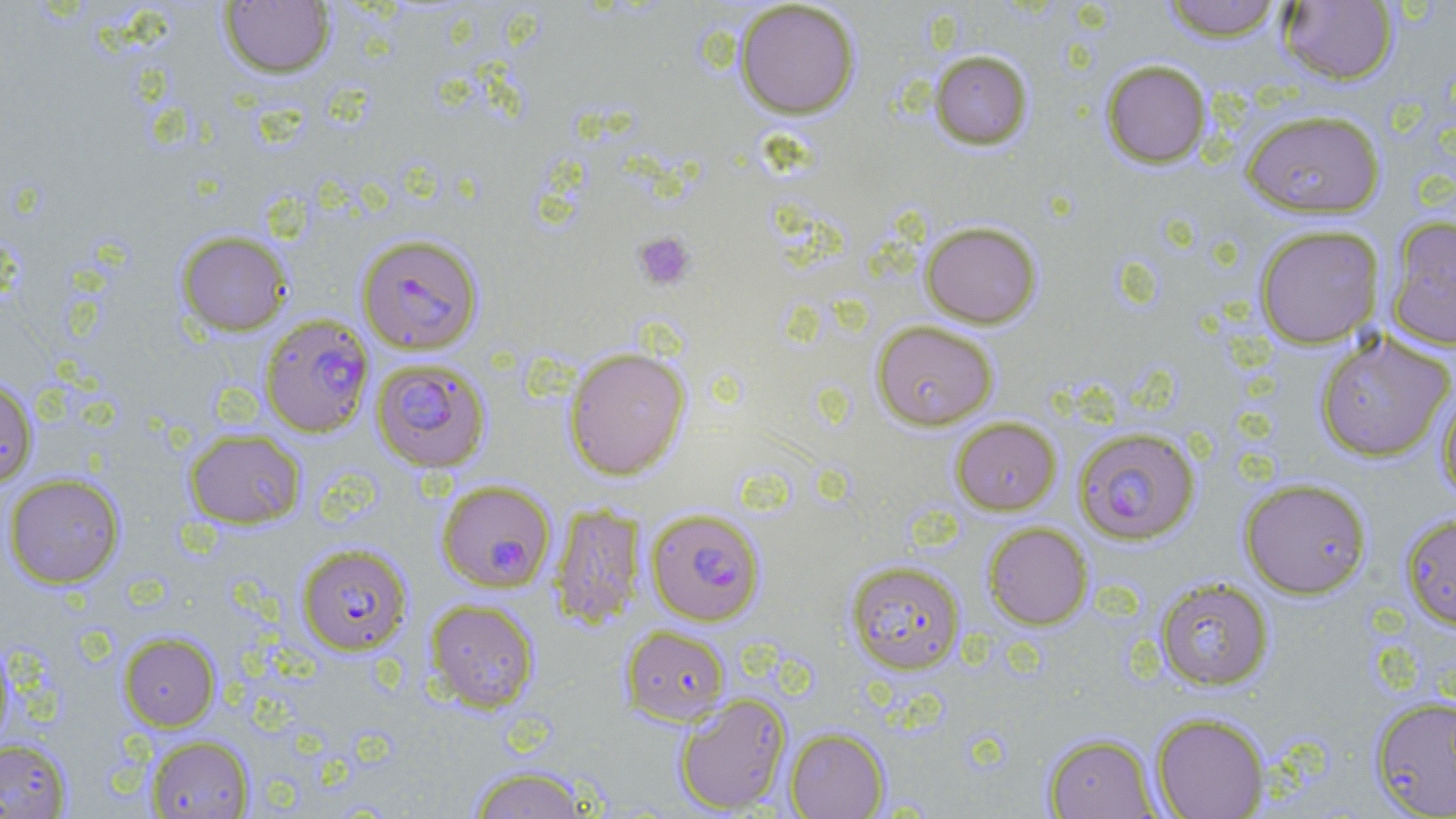

Approximate bounding boxes as (x1, y1, x2, y2) in pixels. Uninfected red blood cell locations: (1160, 0, 1285, 42), (218, 1, 336, 79), (734, 1, 860, 119), (1277, 1, 1399, 85), (929, 49, 1034, 149), (1101, 59, 1212, 168), (1240, 108, 1386, 218), (1385, 216, 1456, 350), (920, 221, 1042, 328), (1253, 224, 1385, 348), (176, 230, 293, 336), (871, 320, 999, 430), (1314, 330, 1455, 462), (564, 346, 691, 480), (0, 376, 39, 488), (1436, 382, 1456, 504), (950, 416, 1061, 515), (183, 428, 307, 529), (3, 474, 125, 588), (1238, 477, 1373, 599), (549, 503, 645, 629), (1399, 512, 1456, 631), (982, 522, 1093, 630), (845, 560, 966, 674), (1154, 577, 1274, 690), (424, 599, 540, 712), (620, 625, 730, 724), (118, 631, 220, 731), (0, 639, 14, 754), (674, 693, 792, 814), (1369, 695, 1456, 818), (1150, 711, 1269, 819), (785, 727, 889, 818), (1041, 732, 1160, 818), (145, 734, 254, 818), (0, 738, 72, 817), (465, 765, 595, 818). Platelet locations: (633, 231, 696, 291). Plasmodium falciparum-infected red blood cell locations: (356, 232, 484, 355), (259, 314, 375, 438), (370, 357, 491, 473), (1073, 426, 1201, 545), (437, 479, 556, 593), (645, 508, 765, 626), (295, 543, 413, 655). Slide-level diagnosis: Plasmodium falciparum. Captured at 1000x magnification. Single field of view. May-Grünwald-Giemsa-stained preparation. Light microscopy. Image is 1456×819 pixels. Thin blood film.